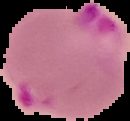
Image is 130×121 pixels. The area outside the segmented cell region is set to black. Result: malaria parasites detected. From a thin blood film.